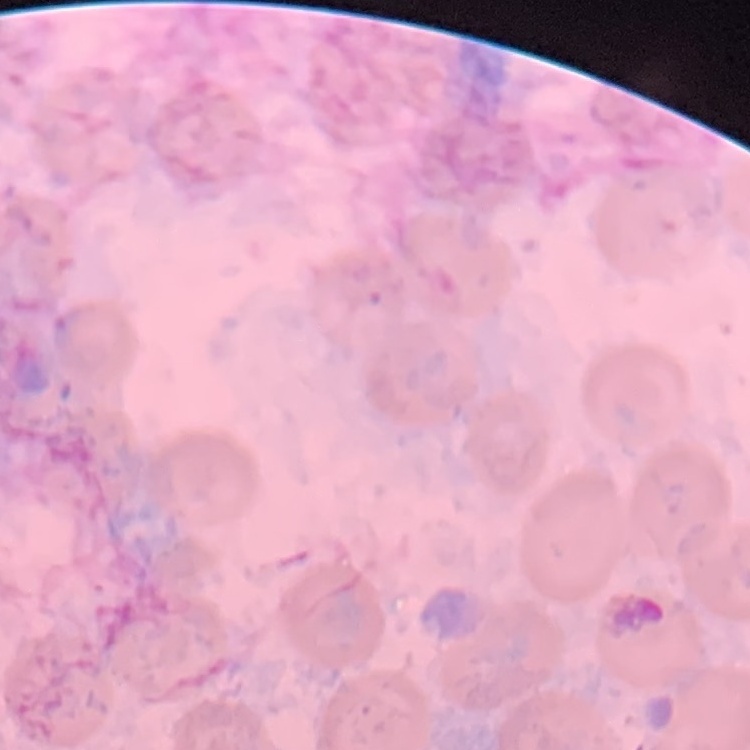
red blood cell morphology = no rouleaux formation
image type = one tile cut from a larger photomicrograph
stain = Field's or Giemsa
preparation = thin blood smear